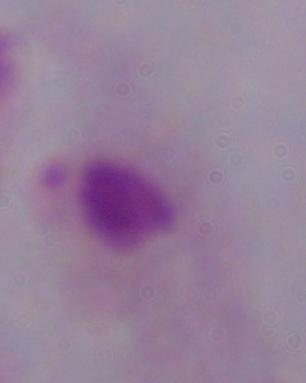

Photomicrograph. Captured at 1000x magnification. A trichomonad is seen.